State the blood parasite species.
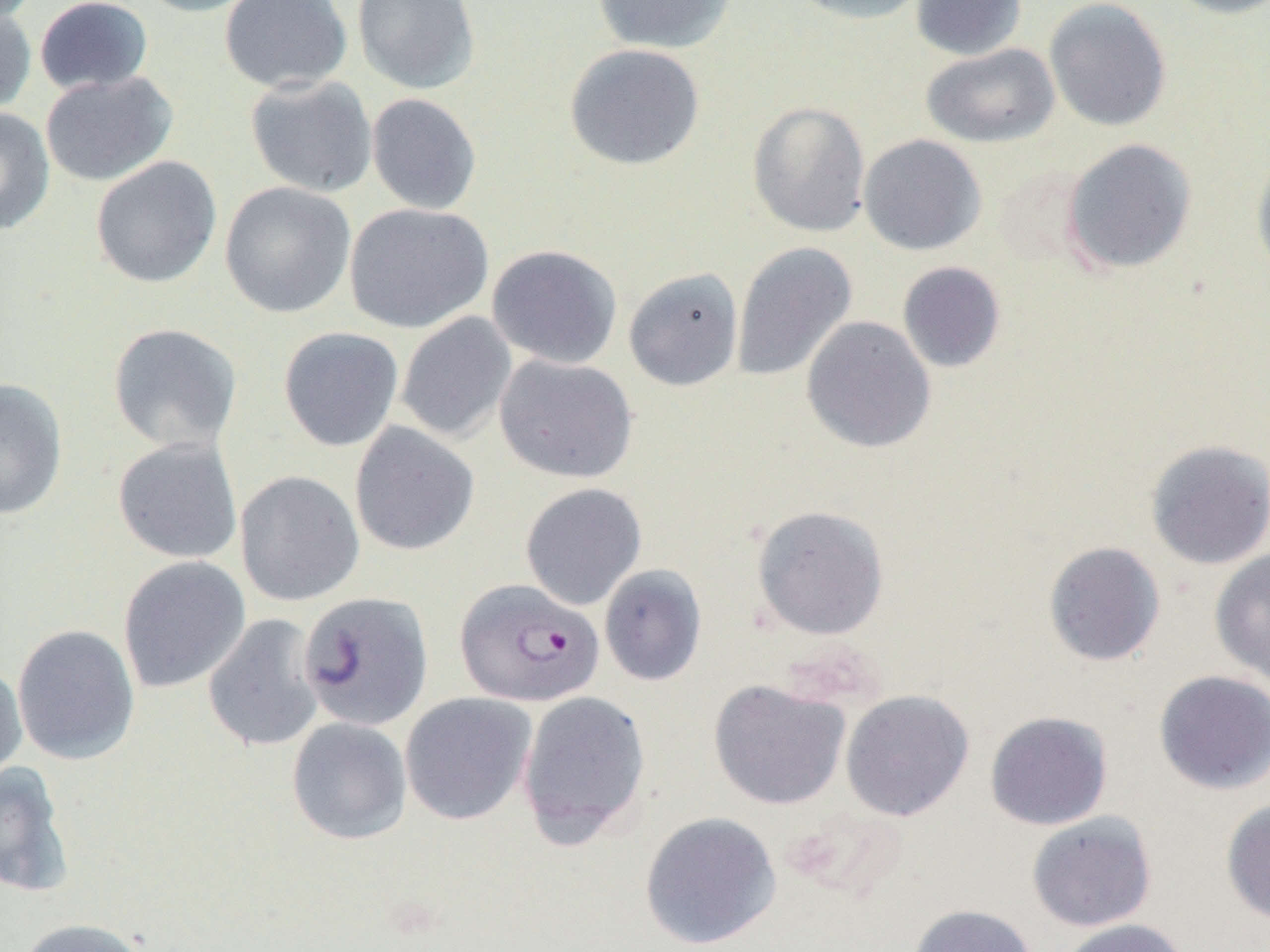
Plasmodium falciparum.

field_of_view: one of a larger specimen
plasmodium_falciparum_infected_red_blood_cell_locations: 'approximate bounding boxes as (x1, y1, x2, y2) in pixels: (454, 578, 604, 707)'
modality: light microscopy
magnification: 1000x
preparation: thin blood film
image_size: 1270×952 pixels
uninfected_red_blood_cell_locations: 'approximate bounding boxes as (x1, y1, x2, y2) in pixels: (34, 0, 154, 96), (132, 0, 267, 17), (219, 0, 352, 93), (352, 0, 481, 94), (592, 0, 736, 54), (787, 0, 931, 25), (910, 0, 1028, 60), (1043, 0, 1172, 132), (1164, 0, 1270, 19), (0, 6, 37, 118), (564, 43, 705, 171), (921, 43, 1060, 148), (39, 71, 178, 186), (245, 75, 378, 197), (366, 93, 482, 215), (747, 101, 871, 237), (0, 107, 55, 236), (858, 134, 987, 256), (1061, 138, 1198, 275), (1251, 149, 1270, 282), (90, 155, 223, 289), (219, 181, 357, 319), (343, 202, 493, 334), (731, 241, 858, 382), (486, 244, 623, 369), (897, 261, 1006, 373), (623, 267, 744, 391), (395, 312, 517, 443), (801, 316, 937, 454), (106, 323, 243, 454), (278, 327, 404, 452), (494, 354, 639, 483), (0, 378, 68, 520), (349, 421, 480, 556), (112, 437, 243, 564), (1144, 439, 1270, 571), (235, 470, 364, 606), (520, 482, 647, 610), (751, 504, 890, 641), (1043, 541, 1166, 666), (1209, 548, 1270, 685), (118, 556, 251, 693), (599, 564, 707, 686), (298, 591, 434, 731), (202, 614, 325, 753), (12, 624, 140, 765), (0, 661, 28, 785), (1153, 670, 1270, 795), (708, 678, 851, 810), (517, 689, 652, 845), (840, 689, 975, 821), (400, 692, 537, 825), (985, 710, 1113, 830), (286, 717, 413, 845), (0, 761, 75, 899), (1220, 798, 1270, 926), (639, 811, 782, 950), (1026, 812, 1157, 932), (907, 904, 1040, 952), (16, 917, 153, 952), (1055, 918, 1191, 952)'